Give the extent of all Plasmodium ovale-infected red blood cells.
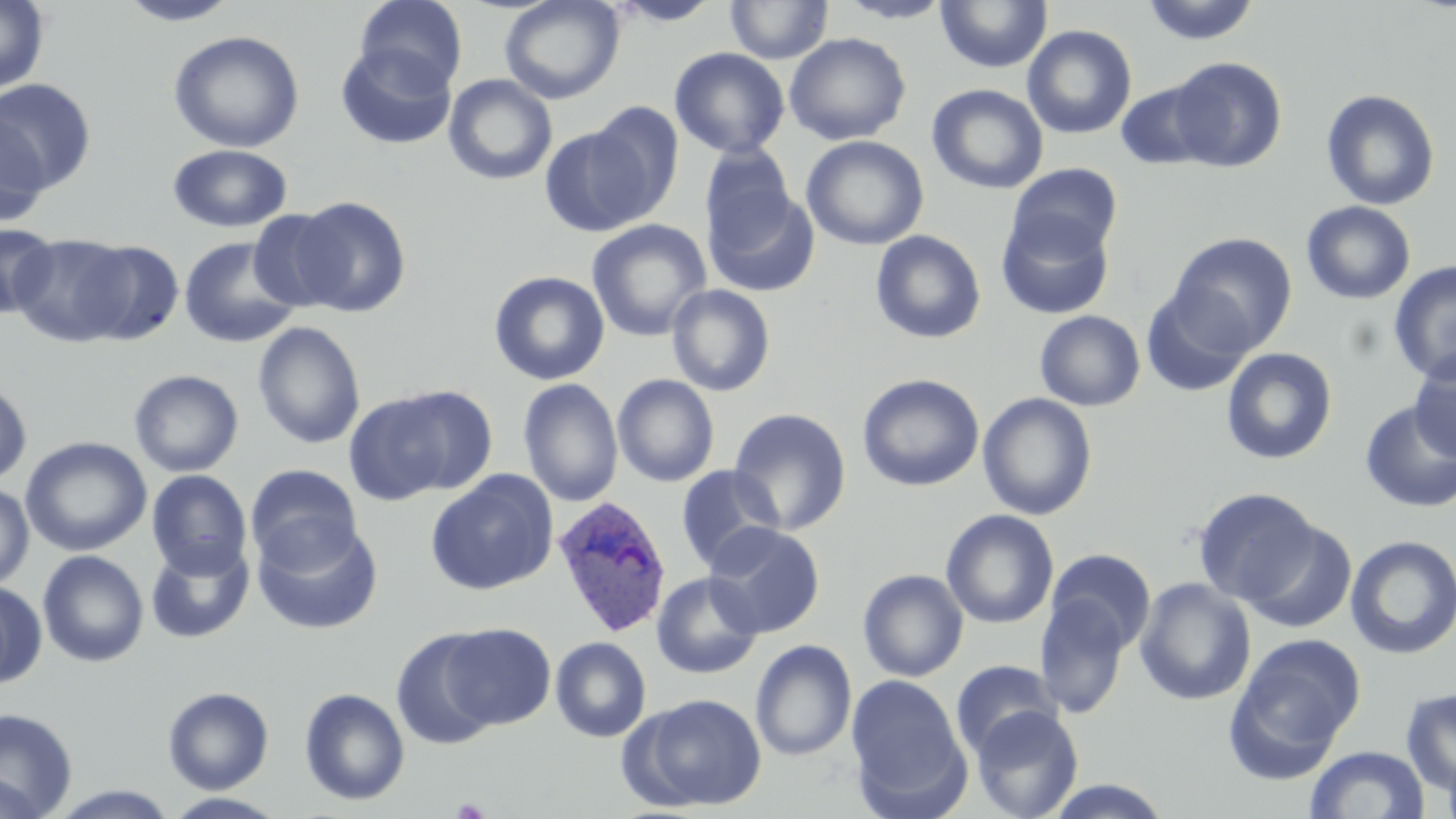
Approximate bounding boxes as [x1, y1, x2, y2] in pixels.
Plasmodium ovale-infected red blood cells: [551, 495, 672, 638].

Summary:
  - Uninfected red blood cell locations: [0, 0, 50, 95], [115, 0, 245, 26], [355, 0, 468, 94], [499, 0, 624, 104], [725, 0, 833, 65], [835, 0, 956, 23], [935, 0, 1053, 73], [1140, 0, 1261, 46], [606, 1, 723, 26], [1022, 24, 1137, 139], [168, 30, 305, 153], [784, 32, 911, 145], [335, 43, 456, 150], [669, 47, 790, 159], [1168, 57, 1287, 173], [443, 74, 558, 185], [0, 79, 97, 193], [1115, 80, 1219, 171], [927, 84, 1049, 194], [1321, 88, 1440, 210], [583, 101, 684, 225], [0, 114, 50, 227], [539, 125, 656, 236], [801, 135, 929, 250], [167, 144, 292, 232], [700, 146, 796, 249], [1008, 163, 1123, 261], [704, 186, 820, 297], [288, 196, 411, 317], [1301, 201, 1416, 305], [247, 209, 347, 311], [995, 209, 1115, 320], [587, 219, 711, 341], [1, 223, 58, 320], [869, 230, 986, 344], [1168, 232, 1298, 354], [10, 234, 137, 346], [179, 236, 302, 348], [73, 240, 185, 344], [1388, 261, 1456, 383], [489, 270, 610, 385], [666, 284, 776, 396], [1141, 289, 1253, 398], [1034, 310, 1145, 411], [252, 321, 366, 450], [1221, 347, 1338, 465], [1409, 352, 1456, 463], [128, 369, 244, 477], [857, 373, 985, 492], [612, 374, 720, 487], [518, 378, 623, 507], [0, 379, 33, 487], [344, 389, 475, 504], [977, 393, 1098, 520], [1358, 398, 1456, 513], [728, 407, 851, 534], [20, 436, 152, 557], [245, 463, 363, 572], [675, 465, 784, 573], [147, 470, 252, 579], [425, 470, 559, 596], [0, 481, 34, 590], [1192, 487, 1322, 607], [940, 509, 1060, 629], [253, 520, 383, 634], [1242, 521, 1357, 633], [703, 522, 825, 638], [1344, 534, 1456, 660], [145, 541, 255, 644], [1045, 549, 1156, 653], [37, 550, 149, 667], [858, 569, 969, 682], [651, 572, 763, 679], [1135, 577, 1256, 706], [0, 580, 46, 689], [1035, 597, 1131, 719], [440, 623, 555, 729], [392, 629, 503, 750], [1228, 633, 1366, 770], [550, 636, 651, 742], [750, 639, 857, 761], [951, 660, 1061, 759], [846, 674, 969, 813], [162, 687, 274, 794], [298, 687, 410, 806], [1400, 687, 1456, 796], [629, 694, 767, 812], [971, 705, 1084, 819], [0, 709, 78, 818], [1305, 745, 1430, 818], [0, 770, 43, 819], [1040, 779, 1175, 818], [43, 784, 182, 817], [161, 792, 290, 818]
  - Platelet locations: [452, 797, 490, 819]
  - Slide-level diagnosis: Plasmodium ovale
  - Stain: May-Grünwald-Giemsa
  - Modality: optical microscopy
  - Magnification: 1000x
  - Preparation: thin blood smear
  - Field of view: one of a larger specimen
  - Image size: 1456×819 pixels